Give the extent of all Plasmodium parasites.
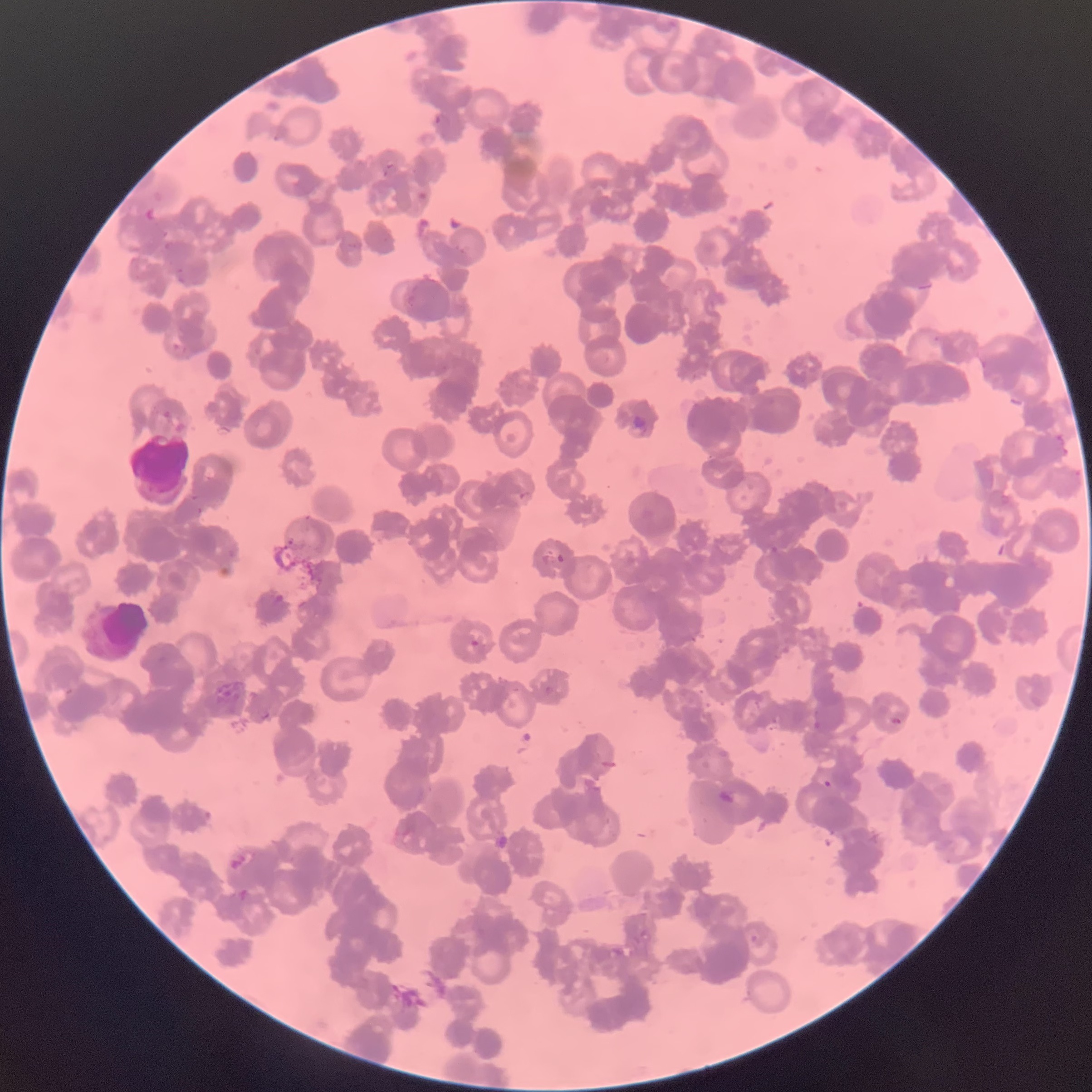

Approximate bounding boxes as [x1, y1, x2, y2] in pixels.
Plasmodium parasites: [435, 113, 450, 128], [933, 336, 941, 343], [556, 552, 566, 563], [471, 639, 488, 659], [544, 685, 554, 696], [890, 716, 902, 727], [822, 779, 832, 789].

Summary:
  - Red blood cell morphology: rouleaux formation
  - Preparation: thin blood film
  - Image size: 1092×1092 pixels
  - Modality: optical microscopy